State the preparation type.
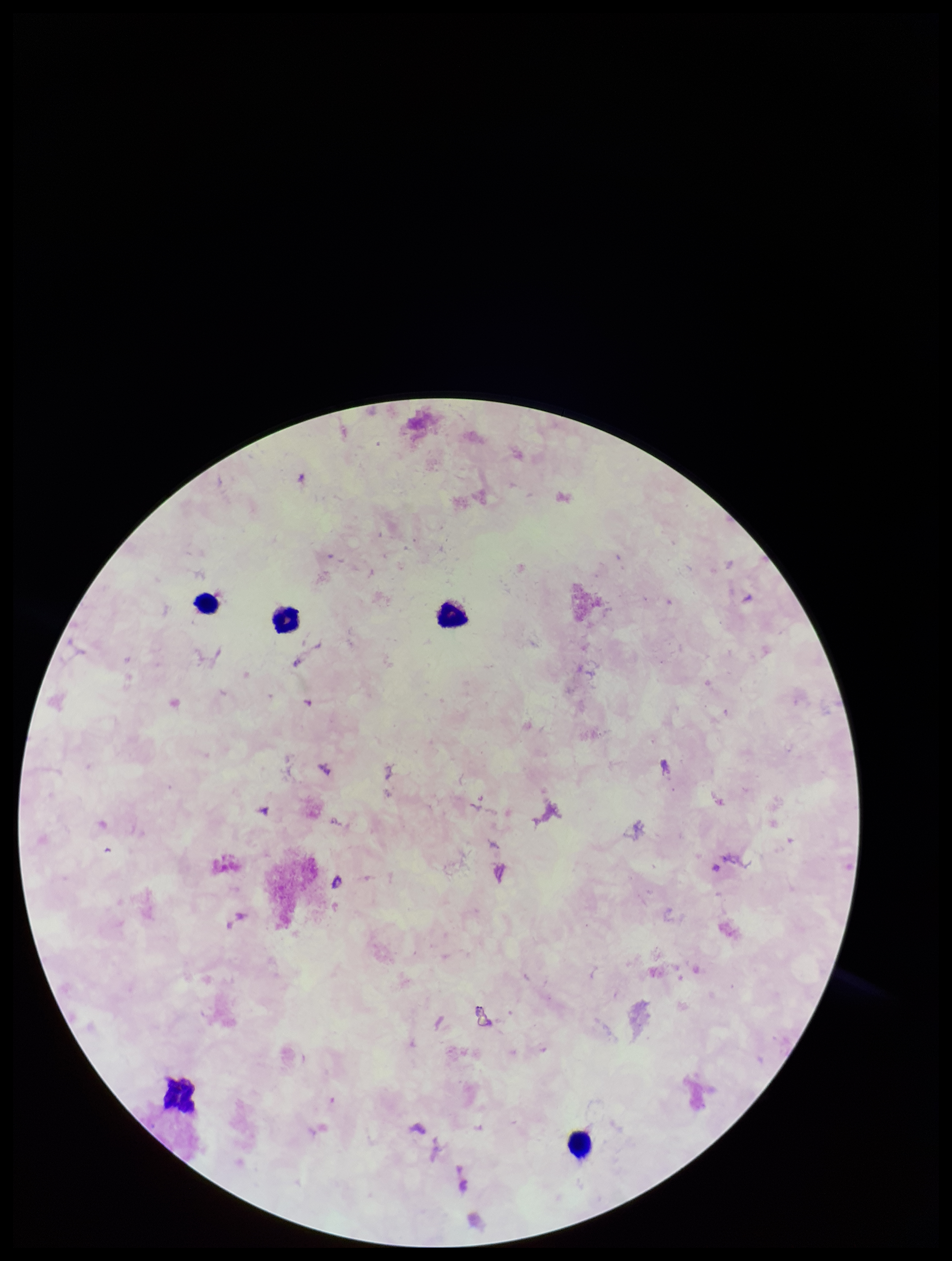
It is a thick blood smear.

Giemsa stain. Single field of view. Image is 952×1261 pixels. Plasmodium parasites: none identified. Patient malaria status: negative. Leukocyte count: 5. Parasite count: 0. Smartphone photograph taken through the eyepiece of a microscope.